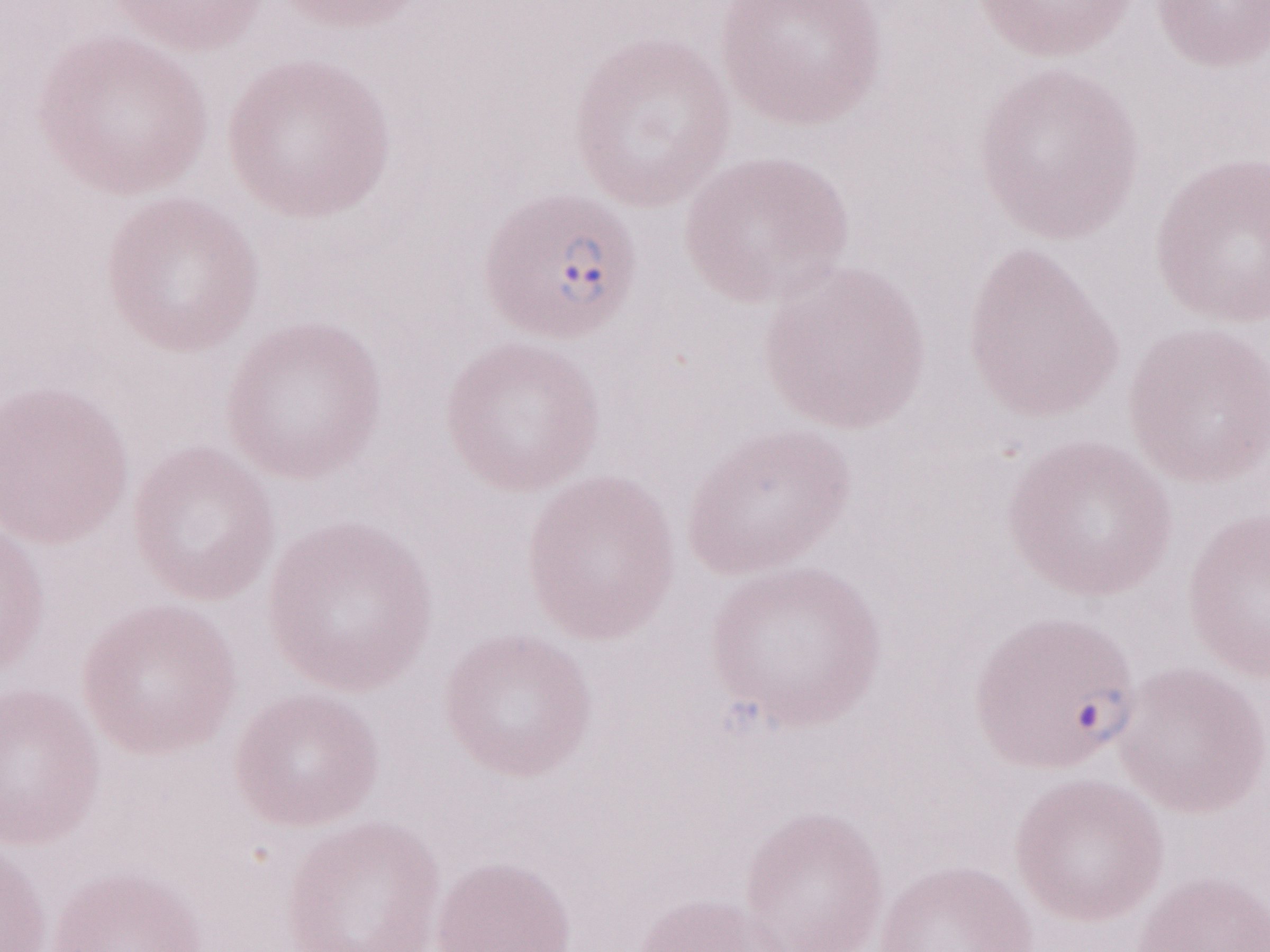
Olympus BX43 microscope, Olympus DP73 camera. Magnification: 1,000x. May-Grünwald-Giemsa stain. Thin blood smear. One field of this slide. Patient diagnosis: malaria infection. Image is 1270×952 pixels.